Point out each leukocyte.
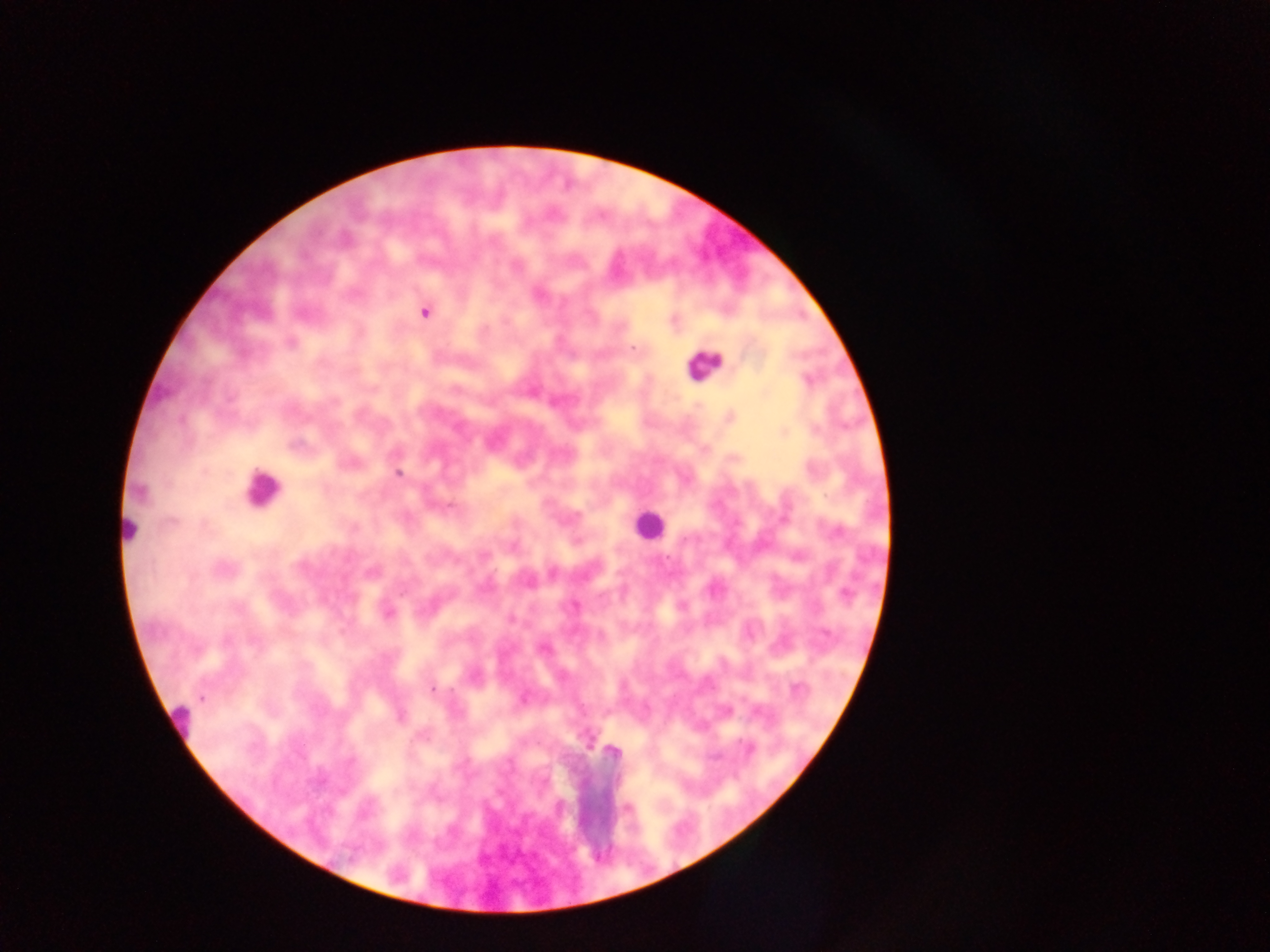

Approximate centers as {x, y} in pixels.
Leukocytes: {265, 486}, {643, 526}.

Plasmodium parasite locations: {553, 213}, {631, 347}, {667, 556}, {432, 687}, {200, 699}. Thick blood smear. Image is 1270×952 pixels. One field of view. Photographed through a microscope with a mobile-phone camera. Collected in Ghana.